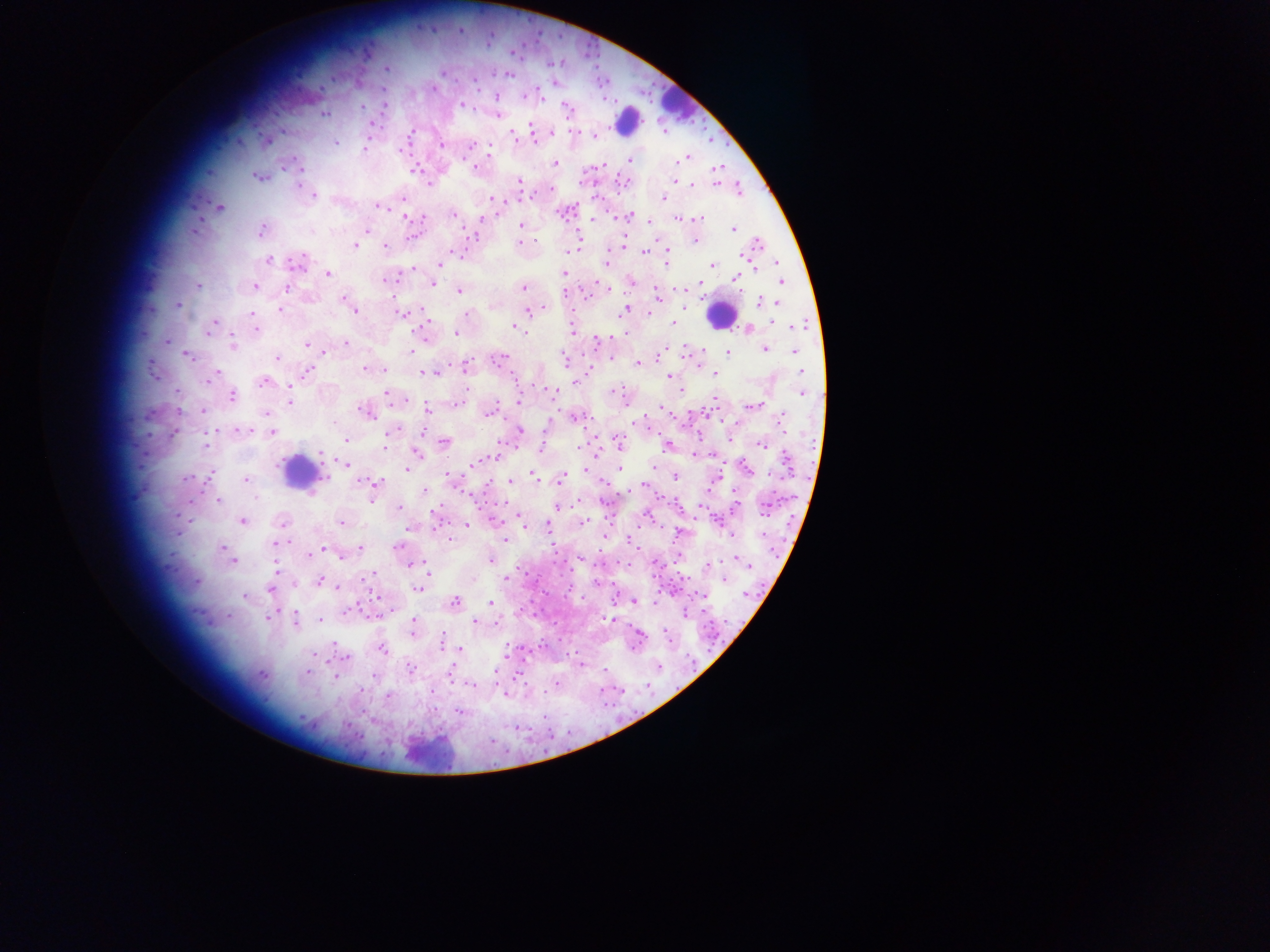

Approximate centers as (x, y) in pixels. Leukocyte locations: (675, 104), (627, 120), (720, 314), (298, 470), (428, 748). Plasmodium parasite locations: (387, 68), (443, 72), (433, 88), (497, 96), (462, 105), (362, 106), (566, 107), (324, 114), (499, 114), (372, 124), (531, 127), (532, 131), (552, 131), (513, 133), (411, 134), (594, 136), (534, 138), (335, 143), (442, 145), (471, 145), (489, 147), (365, 149), (683, 158), (630, 160), (554, 163), (301, 168), (475, 168), (717, 168), (256, 176), (674, 181), (519, 182), (430, 184), (692, 184), (297, 185), (551, 189), (314, 196), (664, 198), (492, 199), (378, 206), (219, 207), (453, 215), (632, 217), (407, 218), (679, 218), (698, 219), (521, 225), (193, 230), (733, 230), (261, 231), (367, 231), (696, 240), (520, 242), (758, 244), (355, 245), (384, 246), (569, 251), (668, 251), (452, 252), (644, 253), (269, 260), (297, 261), (440, 262), (667, 262), (605, 264), (777, 264), (713, 266), (564, 273), (327, 274), (737, 279), (385, 280), (781, 281), (632, 282), (432, 284), (198, 286), (255, 286), (288, 287), (523, 287), (606, 288), (459, 291), (565, 293), (656, 296), (344, 300), (759, 302), (777, 303), (178, 305), (349, 306), (685, 306), (543, 308), (353, 309), (625, 309), (280, 310), (528, 312), (252, 313), (649, 313), (400, 314), (466, 315), (214, 323), (673, 323), (797, 326), (212, 327), (517, 328), (572, 329), (748, 329), (255, 330), (456, 333), (596, 342), (346, 343), (232, 344), (306, 345), (765, 349), (703, 350), (322, 351), (412, 351), (795, 351), (728, 352), (661, 353), (187, 355), (277, 358), (501, 359), (565, 359), (612, 359), (639, 363), (466, 365), (365, 369), (152, 370), (384, 370), (308, 371), (801, 371), (428, 373), (715, 374), (668, 377), (210, 379), (263, 382), (575, 382), (681, 390), (551, 392), (802, 393), (388, 394), (232, 395), (290, 399), (519, 402), (755, 405), (427, 408), (203, 411), (366, 412), (266, 413), (489, 413), (783, 419), (635, 422), (245, 429), (520, 429), (272, 433), (391, 433), (346, 439), (618, 441), (444, 442), (502, 444), (760, 444), (579, 447), (541, 449), (417, 453), (787, 461), (409, 462), (344, 463), (475, 464), (746, 467), (406, 469), (585, 469), (620, 469), (449, 475), (534, 476), (326, 477), (562, 477), (675, 477), (187, 479), (246, 480), (511, 481), (363, 483), (377, 483), (642, 485), (424, 491), (256, 497), (218, 501), (399, 508), (556, 508), (764, 509), (521, 519), (243, 522), (282, 523), (341, 523), (584, 523), (467, 524), (548, 527), (504, 540), (275, 543), (397, 547), (222, 548), (360, 548), (320, 550), (309, 554), (340, 557), (736, 558), (490, 560), (233, 562), (414, 564), (709, 566), (276, 571), (372, 574), (506, 578), (725, 579), (319, 581), (197, 582), (337, 586), (417, 589), (271, 590), (702, 595), (245, 596), (634, 601), (454, 603), (490, 603), (347, 611), (270, 617), (295, 620), (321, 620), (474, 621), (413, 626), (441, 642), (460, 648), (382, 649), (347, 659), (410, 668), (307, 673), (261, 674), (335, 677), (470, 685), (388, 696). One field of view. Thick blood film. Mobile-phone photograph taken through the microscope. Sample from Ghana. Image is 1270×952 pixels.